Locate every blood parasite and identify its species.
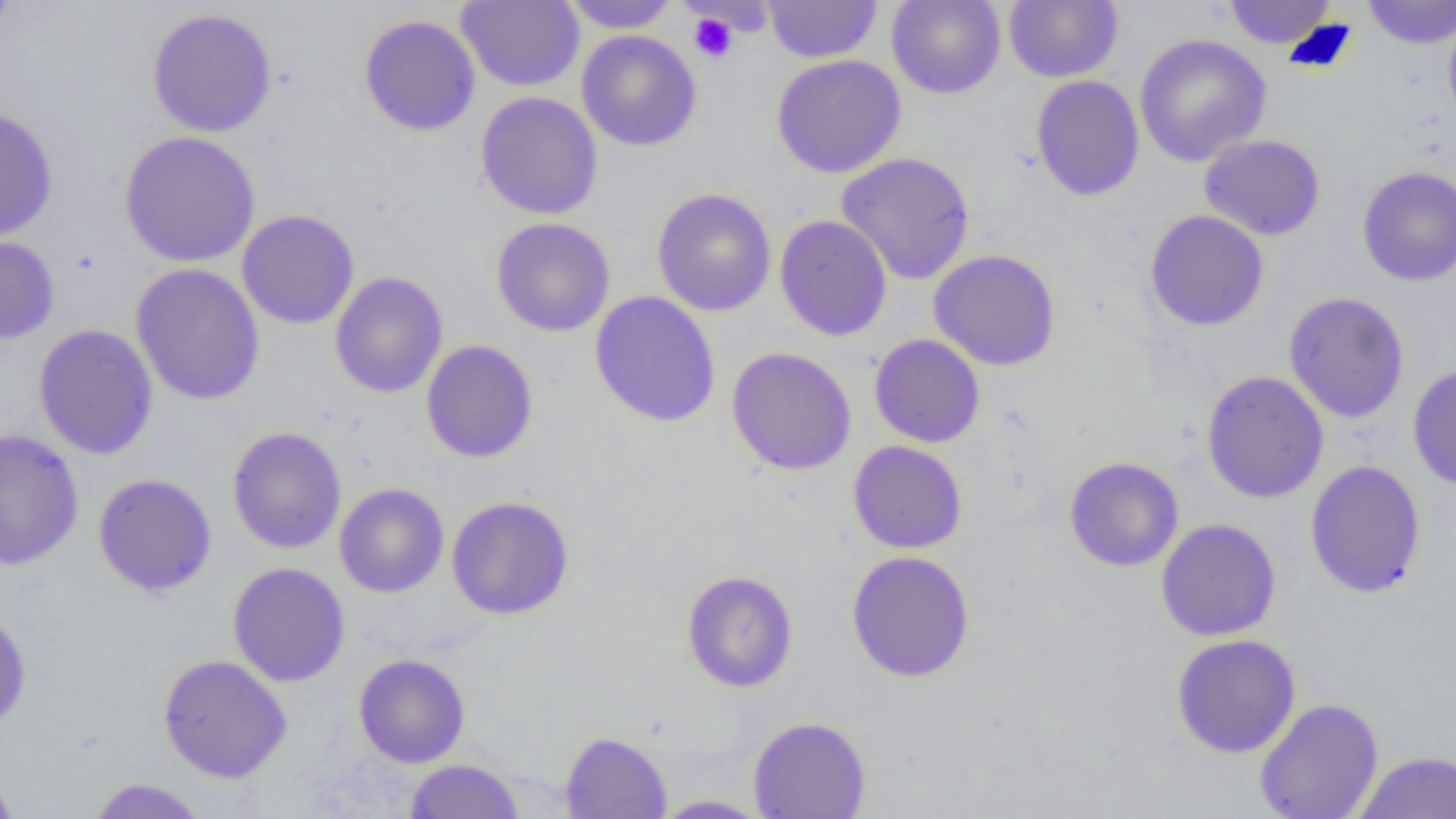
No blood parasites seen.

Summary:
  - Coordinate format: approximate bounding boxes as (x1, y1, x2, y2) in pixels
  - Platelet locations: (688, 12, 738, 63)
  - Uninfected red blood cell locations: (0, 0, 17, 46), (561, 0, 680, 32), (887, 0, 1006, 99), (1004, 0, 1123, 83), (1222, 0, 1337, 49), (1362, 0, 1456, 49), (456, 1, 584, 91), (763, 1, 882, 63), (146, 8, 277, 138), (1443, 13, 1456, 132), (359, 14, 482, 137), (577, 30, 701, 152), (1134, 33, 1272, 167), (771, 54, 907, 179), (1030, 75, 1145, 202), (476, 91, 603, 220), (0, 106, 59, 241), (119, 131, 260, 268), (1199, 134, 1326, 241), (836, 152, 976, 285), (1357, 166, 1456, 286), (652, 188, 776, 317), (237, 210, 360, 329), (1144, 210, 1269, 332), (775, 215, 893, 342), (491, 217, 616, 337), (0, 235, 60, 345), (928, 249, 1061, 371), (130, 263, 266, 405), (330, 272, 448, 399), (1283, 291, 1410, 424), (589, 292, 721, 428), (33, 324, 159, 460), (869, 334, 985, 448), (421, 340, 538, 464), (726, 346, 857, 475), (1408, 365, 1456, 491), (1201, 371, 1329, 503), (227, 426, 346, 554), (0, 429, 84, 570), (848, 441, 967, 554), (1065, 456, 1184, 572), (1304, 460, 1427, 598), (92, 473, 218, 596), (334, 483, 449, 598), (446, 495, 575, 620), (1155, 518, 1281, 641), (846, 550, 976, 683), (228, 562, 350, 687), (681, 570, 798, 692), (0, 606, 32, 732), (1171, 634, 1301, 758), (353, 653, 471, 768), (158, 654, 293, 783), (1254, 697, 1383, 819), (748, 715, 871, 818), (560, 731, 672, 819), (1354, 751, 1456, 819), (403, 758, 525, 818), (0, 767, 20, 818), (86, 777, 210, 818), (650, 794, 773, 817)
  - Slide-level diagnosis: no evidence of blood parasites
  - Modality: light microscopy
  - Magnification: 1000x
  - Field of view: one of a larger specimen
  - Preparation: thin blood smear
  - Image size: 1456×819 pixels